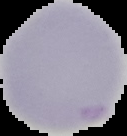
Malaria status: uninfected. From a thin blood smear. Image is 127×136 pixels. The area outside the segmented cell region is set to black.